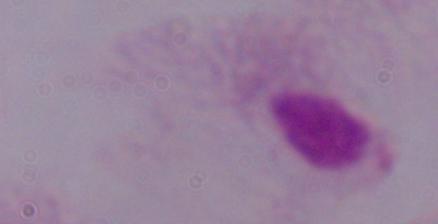
magnification = 1000x
modality = micrograph
identification = trichomonad